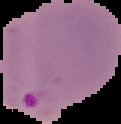
image size = 121×124 pixels
preparation = thin blood smear
malaria status = parasitized
image type = segmented cell region with the area outside set to black